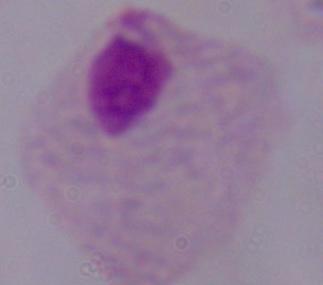
magnification = 1000x
modality = photomicrograph
identification = trichomonad